Outline each blood parasite and name the species.
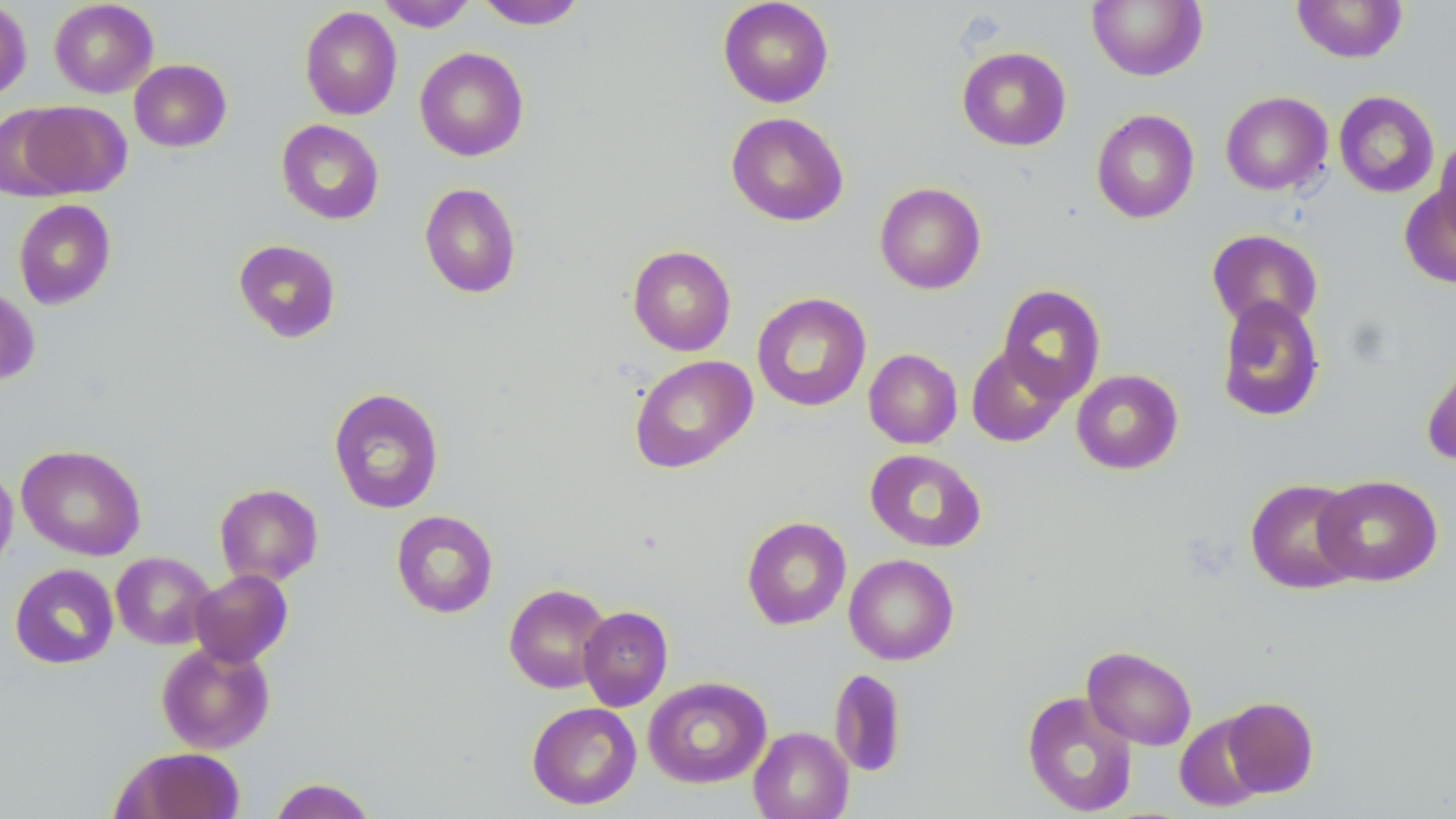
No blood parasites seen.

slide_level_diagnosis: no evidence of blood parasites
magnification: 1000x
image_size: 1456×819 pixels
uninfected_red_blood_cell_locations: 'approximate bounding boxes as (x1,y1)-(x2,y2) corner pairs in pixels: (49,0)-(158,98), (376,0)-(478,32), (718,0)-(834,108), (1086,0)-(1207,81), (1291,0)-(1408,63), (0,1)-(32,101), (475,1)-(587,29), (299,6)-(402,120), (957,46)-(1072,151), (414,47)-(529,161), (129,59)-(232,152), (1220,91)-(1332,196), (1334,91)-(1439,198), (14,100)-(131,199), (1091,109)-(1199,224), (726,111)-(849,226), (276,119)-(384,225), (1433,133)-(1456,246), (874,182)-(986,294), (1399,182)-(1456,290), (419,183)-(521,298), (13,199)-(116,310), (1206,229)-(1323,331), (233,239)-(341,343), (627,245)-(736,356), (996,284)-(1106,403), (0,285)-(40,386), (752,293)-(871,412), (1215,296)-(1326,422), (966,344)-(1071,447), (1420,347)-(1456,468), (864,348)-(962,449), (629,355)-(757,473), (1071,369)-(1183,475), (328,387)-(444,514), (16,444)-(146,560), (865,449)-(987,553), (0,462)-(18,576), (1314,474)-(1443,587), (1245,478)-(1364,594), (214,483)-(324,586), (391,510)-(498,618), (742,516)-(851,630), (111,551)-(216,650), (844,553)-(959,665), (9,563)-(119,669), (190,569)-(293,667), (504,583)-(612,693), (578,606)-(673,711), (156,641)-(275,754), (1082,645)-(1197,751), (829,668)-(907,777), (643,676)-(771,788), (1022,691)-(1138,816), (1222,696)-(1320,797), (526,701)-(642,809), (1174,713)-(1269,812), (749,726)-(853,819), (113,747)-(246,819), (268,777)-(378,819)'
modality: light microscopy
field_of_view: one of a larger specimen
stain: May-Grünwald-Giemsa
preparation: thin blood film